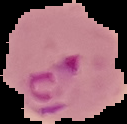
image type = segmented cell region on a black background
malaria status = parasitized
image size = 127×124 pixels
preparation = thin blood film